Identify the parasite.
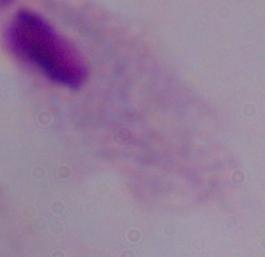
A trichomonad.

Summary:
  - Magnification: 1000x
  - Modality: micrograph